Locate platelets.
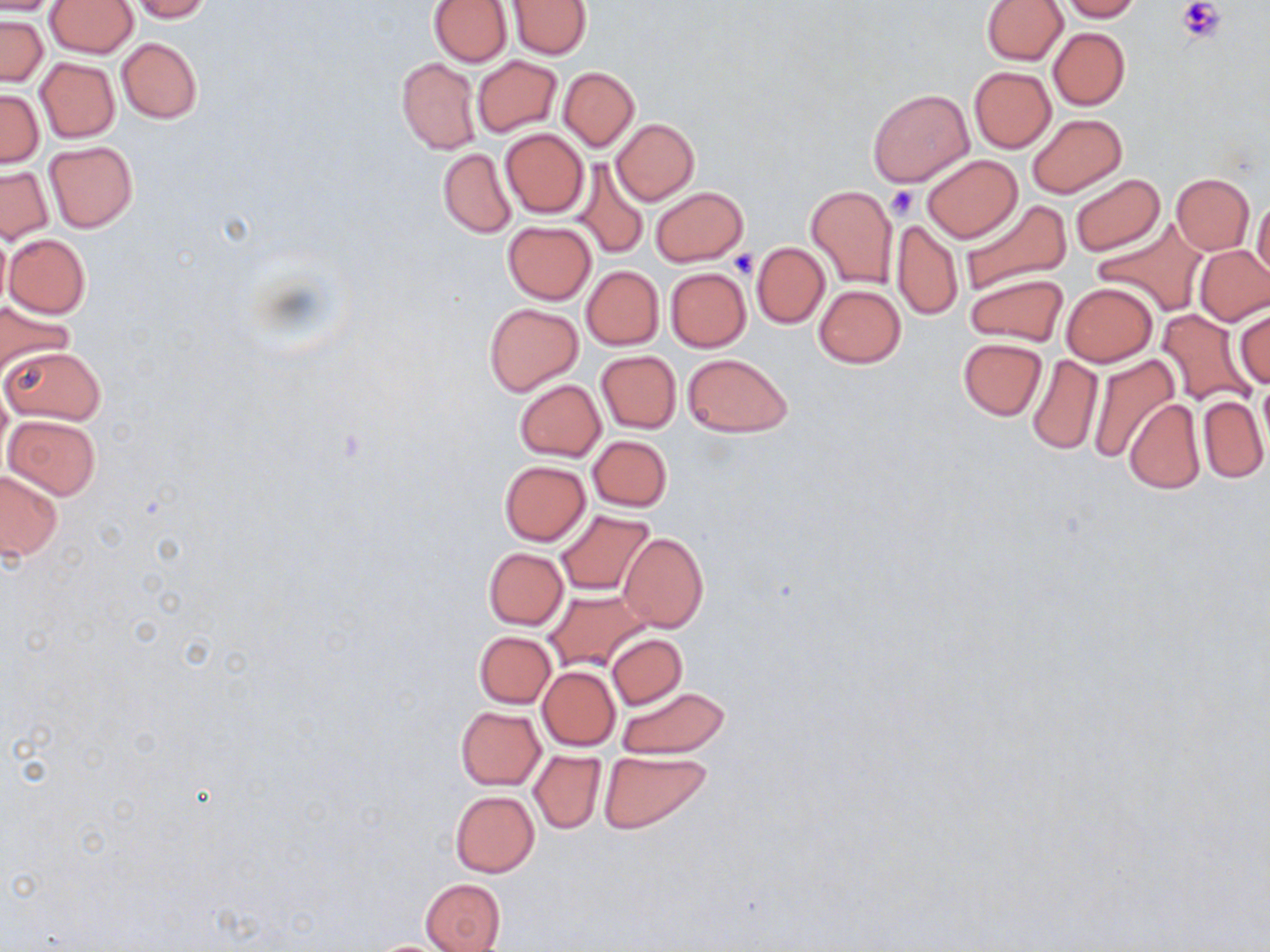

Approximate bounding boxes as [x1, y1, x2, y2] in pixels.
Platelets: [1178, 0, 1224, 44], [886, 186, 919, 219], [729, 249, 755, 281].

Uninfected red blood cell locations: [0, 0, 60, 17], [127, 0, 211, 21], [428, 0, 512, 67], [1059, 0, 1142, 22], [45, 1, 137, 57], [508, 1, 591, 59], [981, 1, 1068, 65], [0, 16, 47, 86], [1048, 27, 1130, 109], [117, 37, 201, 123], [472, 56, 561, 136], [35, 57, 119, 142], [396, 57, 481, 154], [558, 67, 639, 150], [969, 67, 1056, 152], [866, 88, 973, 188], [0, 89, 43, 168], [1025, 114, 1126, 198], [611, 119, 699, 204], [500, 129, 589, 217], [43, 142, 138, 232], [439, 148, 516, 237], [922, 153, 1022, 242], [571, 159, 651, 257], [1, 167, 52, 243], [1170, 173, 1254, 254], [1070, 174, 1164, 257], [806, 184, 898, 287], [651, 186, 747, 266], [1252, 198, 1269, 282], [959, 199, 1072, 298], [892, 220, 963, 321], [1092, 220, 1206, 317], [502, 221, 597, 303], [4, 233, 90, 319], [752, 242, 830, 326], [1195, 245, 1270, 326], [581, 266, 663, 350], [665, 267, 750, 351], [966, 273, 1067, 347], [1061, 282, 1157, 366], [813, 284, 905, 368], [0, 299, 76, 369], [484, 302, 584, 396], [1234, 307, 1269, 392], [1155, 308, 1254, 406], [958, 337, 1047, 420], [1, 345, 106, 425], [595, 350, 681, 433], [682, 353, 794, 436], [1026, 353, 1104, 457], [1086, 353, 1180, 462], [514, 379, 605, 460], [1257, 379, 1270, 454], [1197, 395, 1269, 482], [1125, 398, 1204, 492], [4, 414, 100, 499], [587, 435, 672, 511], [498, 460, 590, 545], [0, 469, 63, 561], [554, 509, 655, 597], [618, 532, 709, 632], [484, 547, 567, 629], [544, 589, 648, 670], [475, 631, 555, 708], [607, 634, 686, 709], [536, 666, 620, 751], [614, 685, 730, 759], [455, 706, 545, 790], [529, 750, 606, 833], [599, 750, 712, 833], [450, 790, 540, 877], [421, 878, 506, 952]. Slide-level diagnosis: negative for blood parasites. Light microscopy. One field of a larger specimen. Image is 1270×952 pixels. Thin blood film. Captured at 1000x magnification. May-Grünwald-Giemsa stain.